Report the malaria status of this cell.
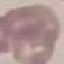
It is uninfected.

Summary:
  - Preparation: thin smear
  - Capture: smartphone through the microscope eyepiece
  - Stain: Giemsa
  - Image type: cell patch, automatically extracted from a larger field of view and resized to 64 × 64 pixels